Classify this cell by malaria status.
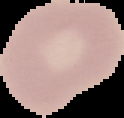

Uninfected.

preparation: thin blood smear
image_type: segmented cell region with the area outside set to black
image_size: 124×118 pixels